Identify the parasite.
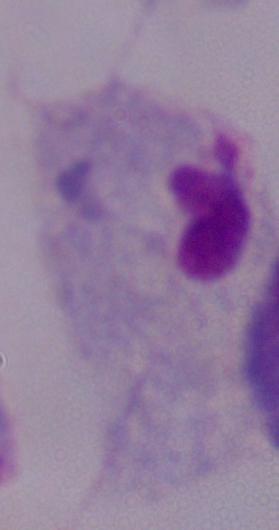

A trichomonad.

{
  "magnification": "1000x",
  "modality": "micrograph"
}